Point out each Plasmodium parasite.
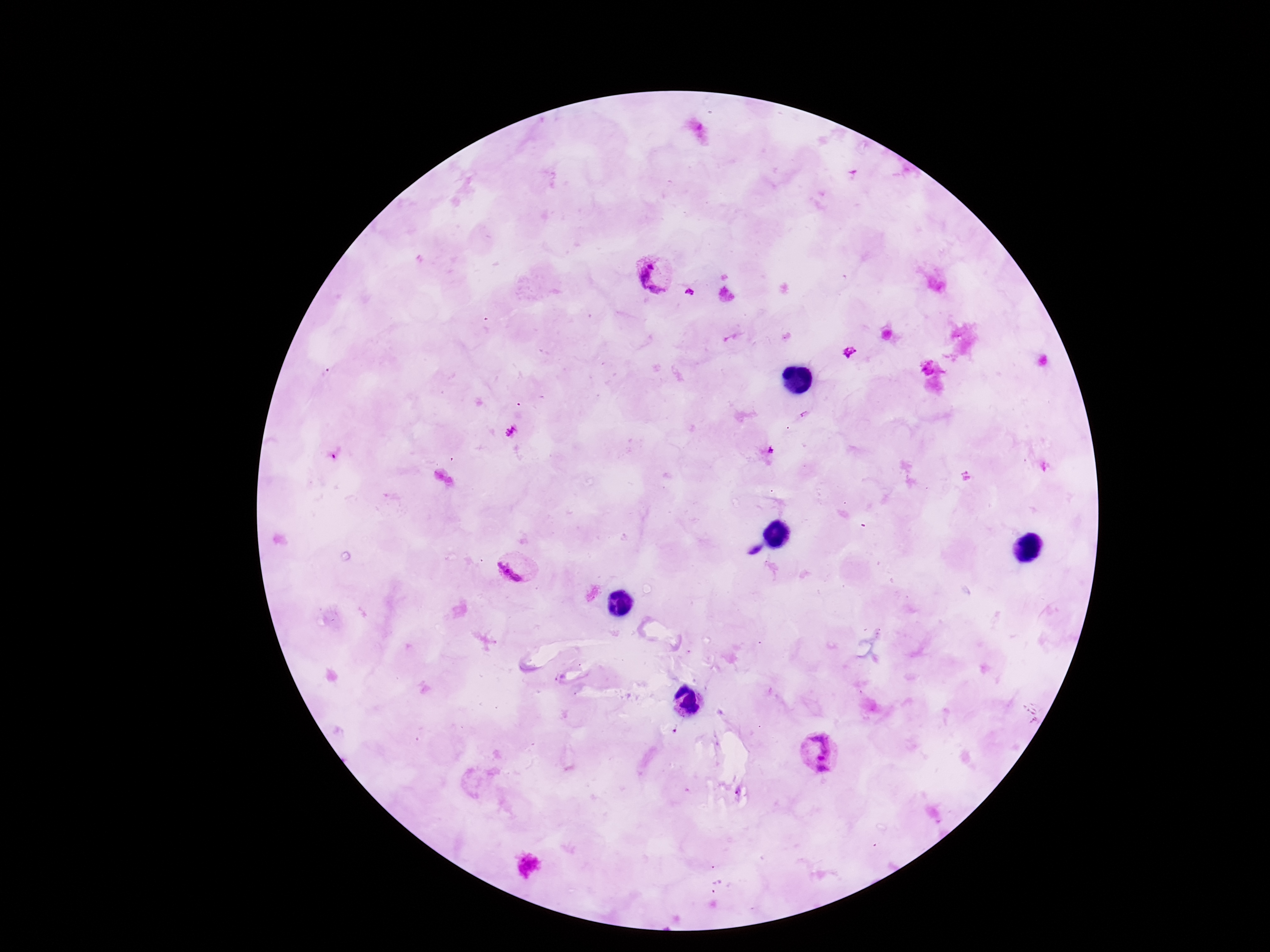
Approximate centers as (x, y) in pixels.
Plasmodium parasites: (655, 275), (690, 292), (849, 352), (511, 431), (771, 450), (516, 567), (818, 752).

preparation = thick peripheral-blood smear
field of view = one from this slide
capture = smartphone camera through the microscope eyepiece
patient malaria status = positive
image size = 1270×952 pixels
stain = Giemsa
magnification = 100x